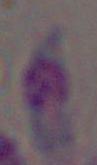

modality: photomicrograph
magnification: 1000x
identification: Toxoplasma gondii